State which parasite is depicted.
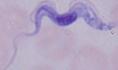

A trypanosome.

Photomicrograph. 1000x magnification.